Name the blood parasite species.
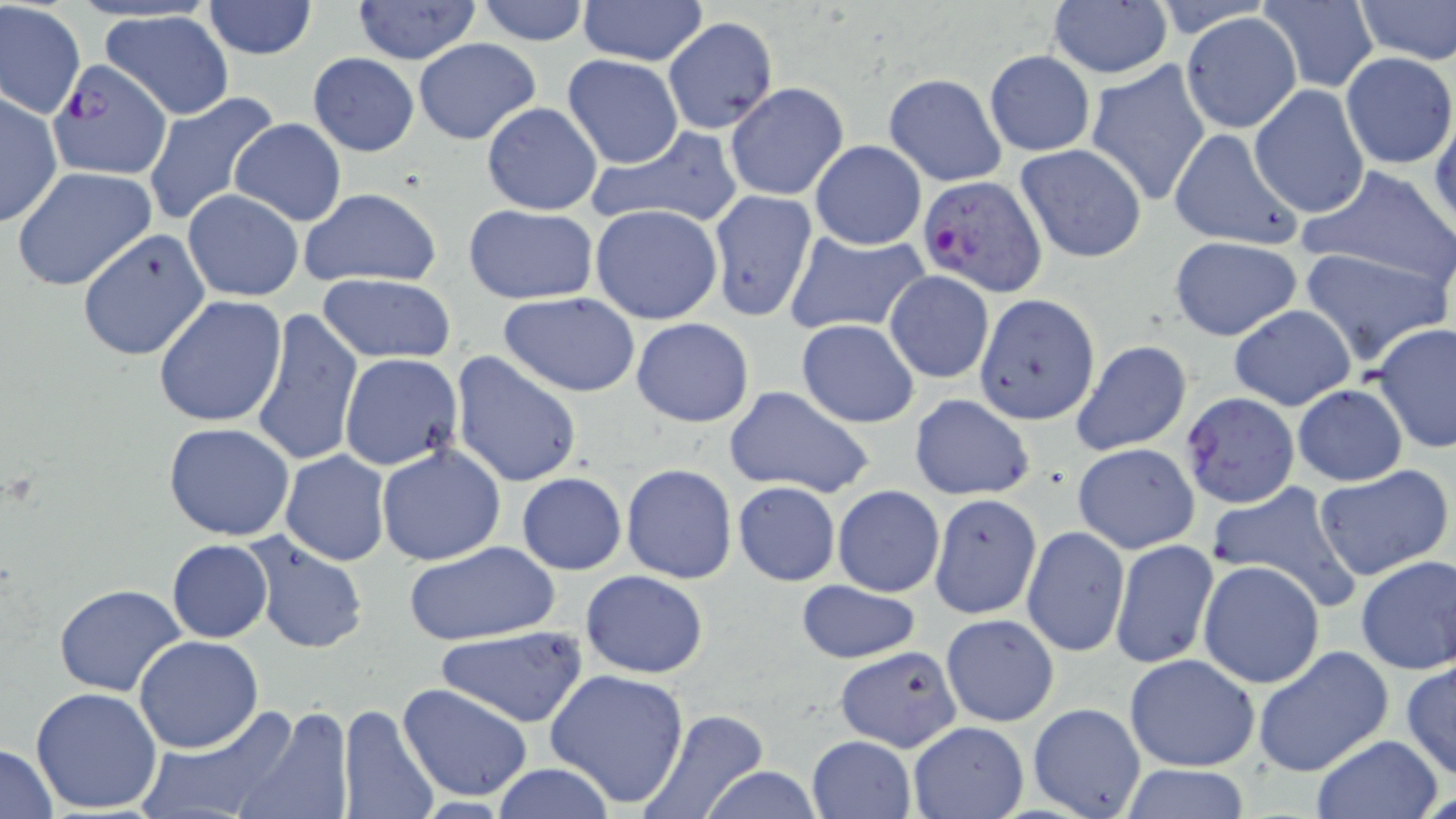
Plasmodium falciparum.

Summary:
  - Coordinate format: approximate bounding boxes as (x1,y1)-(x2,y2) corner pairs in pixels
  - Plasmodium falciparum-infected red blood cell locations: (48,58)-(173,179), (918,174)-(1048,298), (1180,390)-(1301,510)
  - Uninfected red blood cell locations: (353,0)-(481,64), (473,0)-(591,45), (1259,0)-(1378,92), (1352,0)-(1455,64), (578,1)-(707,66), (202,2)-(318,59), (1,3)-(85,118), (1047,3)-(1173,80), (1179,10)-(1303,134), (101,11)-(235,120), (662,18)-(778,134), (413,37)-(542,145), (984,49)-(1095,156), (1341,52)-(1456,170), (308,53)-(419,157), (562,54)-(683,168), (1084,60)-(1211,207), (883,73)-(1007,186), (724,82)-(849,201), (1249,85)-(1370,218), (143,91)-(282,227), (0,92)-(62,229), (481,102)-(603,215), (1430,113)-(1456,232), (230,118)-(347,226), (585,126)-(744,230), (1168,127)-(1303,251), (810,140)-(927,249), (1016,144)-(1146,263), (11,167)-(157,291), (1297,167)-(1456,289), (297,186)-(444,289), (182,190)-(305,301), (708,190)-(819,322), (591,203)-(723,324), (462,204)-(599,305), (76,227)-(210,361), (785,230)-(929,337), (1168,235)-(1303,341), (1298,246)-(1451,365), (884,270)-(994,383), (318,274)-(457,363), (498,292)-(642,396), (973,292)-(1098,426), (154,295)-(288,427), (1230,305)-(1356,411), (250,308)-(363,468), (630,318)-(755,427), (795,319)-(919,427), (1373,322)-(1456,453), (1070,340)-(1193,456), (450,352)-(583,489), (337,353)-(464,471), (723,383)-(876,499), (1293,384)-(1407,487), (908,394)-(1035,500), (164,421)-(295,540), (1076,442)-(1205,551), (375,443)-(506,567), (279,449)-(392,566), (621,463)-(737,583), (1312,465)-(1453,580), (517,472)-(627,574), (458,477)-(612,609), (1206,480)-(1365,615), (732,481)-(840,586), (833,485)-(944,597), (929,494)-(1042,618), (1022,525)-(1129,657), (243,529)-(369,654), (167,539)-(273,642), (1109,539)-(1219,670), (405,540)-(561,647), (1353,553)-(1456,674), (1198,560)-(1325,688), (580,570)-(709,677), (795,580)-(921,663), (53,584)-(187,697), (940,613)-(1059,726), (435,627)-(587,726), (134,636)-(262,753), (835,645)-(963,751), (1250,645)-(1394,777), (1124,654)-(1260,772), (1400,661)-(1456,780), (547,669)-(690,807), (397,683)-(534,802), (31,686)-(164,814), (1028,701)-(1147,819), (338,703)-(440,819), (135,706)-(300,819), (233,706)-(352,819), (640,708)-(769,819), (908,722)-(1028,818), (1308,734)-(1443,818), (805,735)-(915,819), (0,743)-(58,818), (490,762)-(616,818), (1115,763)-(1255,819), (699,764)-(825,819)
  - Stain: May-Grünwald-Giemsa
  - Image size: 1456×819 pixels
  - Field of view: one of a larger specimen
  - Magnification: 1000x
  - Modality: optical microscopy
  - Preparation: thin blood smear